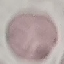
result = negative for malaria parasites
image type = cell patch, automatically extracted from a larger field of view and resized to 64 × 64 pixels
preparation = thin blood film
stain = Giemsa
capture = smartphone camera at the microscope eyepiece